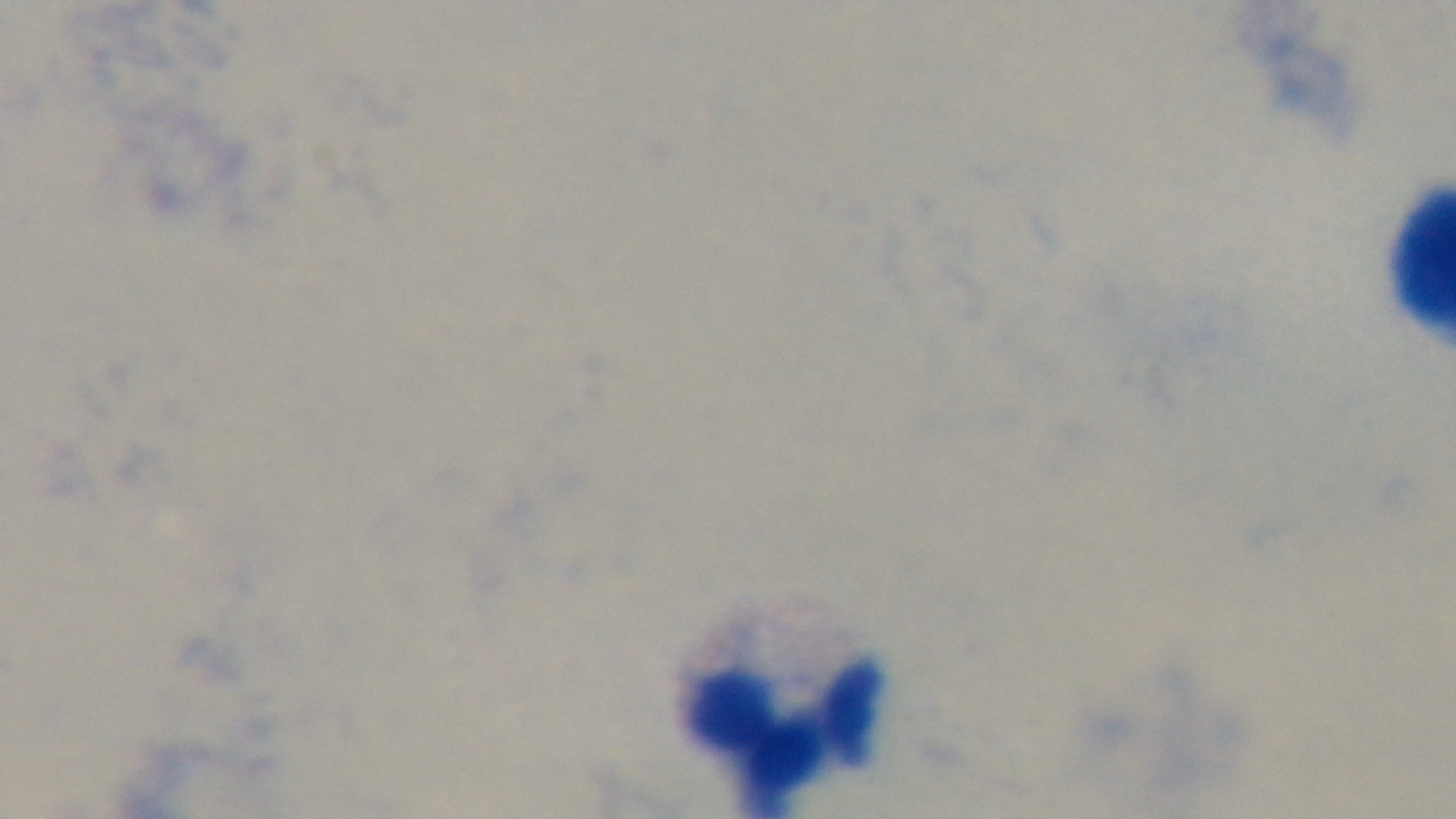
{
  "modality": "light microscopy",
  "stain": "Giemsa",
  "malaria_status": "uninfected",
  "field_of_view": "one from the slide",
  "objective": "100x oil immersion",
  "capture": "mounted 4K digital camera",
  "preparation": "thick"
}